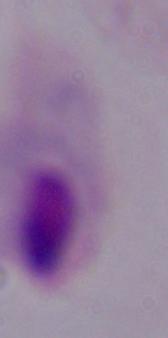

magnification = 1000x
identification = trichomonad
modality = micrograph